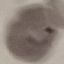

result = malaria parasites detected
stain = Giemsa
capture = smartphone camera at the microscope eyepiece
image type = automatically extracted cell patch, resized to 64 × 64 pixels
preparation = thin smear